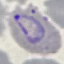
malaria status = parasitized
image type = cell patch, automatically extracted from a larger field of view and resized to 64 × 64 pixels
stain = Giemsa
preparation = thin smear
capture = smartphone through the microscope eyepiece